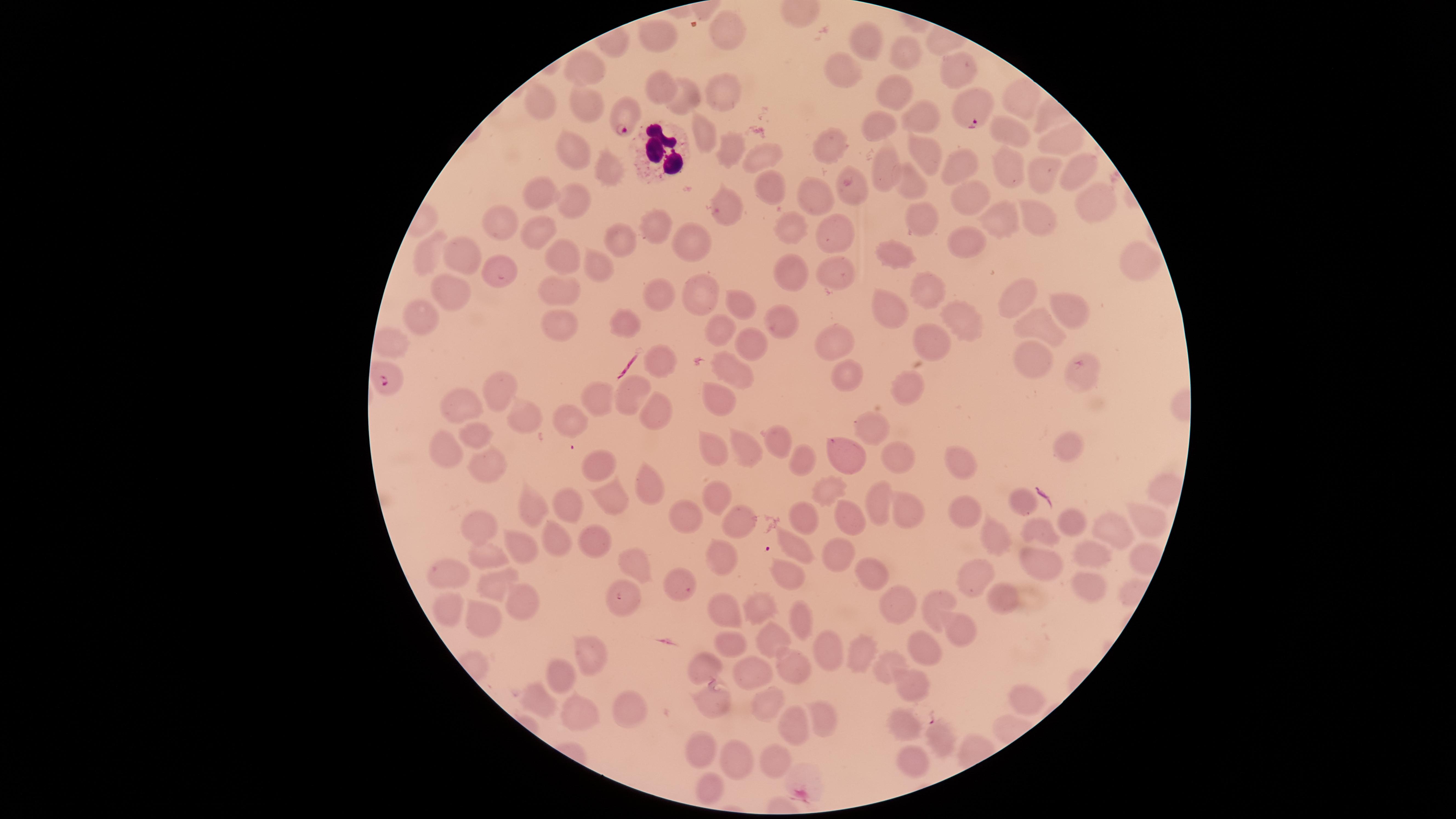
Approximate marker points as [x, y] in pixels. Parasitized RBCs: [970, 108], [623, 114], [388, 384]. Uninfected RBCs: [722, 32], [662, 37], [865, 41], [908, 54], [587, 67], [961, 67], [839, 70], [662, 85], [897, 93], [722, 94], [1019, 96], [685, 97], [538, 102], [588, 102], [923, 112], [1006, 123], [885, 124], [702, 131], [1059, 139], [829, 144], [572, 150], [922, 151], [728, 152], [760, 156], [613, 164], [889, 164], [962, 166], [1011, 169], [1074, 169], [1048, 176], [773, 183], [910, 183], [852, 191], [962, 193], [814, 195], [543, 196], [575, 196], [1100, 199], [724, 208], [1029, 215], [921, 216], [1002, 216], [510, 219], [794, 227], [844, 227], [656, 232], [548, 233], [621, 238], [693, 244], [967, 245], [896, 252], [465, 253], [428, 256], [1137, 257], [560, 261], [790, 265], [504, 267], [601, 269], [833, 274], [560, 290], [455, 292], [925, 292], [660, 293], [703, 293], [1023, 295], [736, 304], [1070, 307], [889, 310], [422, 314], [631, 317], [777, 320], [561, 323], [964, 325], [1040, 327], [719, 328], [834, 338], [752, 339], [925, 339], [392, 344], [1033, 356], [663, 359], [735, 368], [847, 376], [1082, 376], [908, 387], [498, 392], [633, 393], [721, 393], [598, 401], [464, 406], [657, 413], [526, 418], [575, 419], [869, 428], [481, 440], [779, 441], [713, 442], [1073, 447], [446, 449], [748, 451], [848, 456], [894, 460], [959, 460], [806, 462], [490, 463], [599, 466], [647, 485], [829, 490], [612, 494], [721, 497], [875, 498], [1019, 498], [533, 504], [570, 504], [964, 509], [906, 513], [685, 515], [804, 516], [852, 519], [1143, 519], [740, 520], [486, 523], [1068, 523], [553, 533], [1112, 535], [1044, 536], [596, 541], [992, 542], [520, 544], [798, 548], [1090, 553], [837, 554], [1034, 554], [484, 555], [719, 559], [635, 560], [977, 569], [448, 572], [874, 572], [790, 573], [495, 581], [677, 583], [1087, 588], [622, 594], [1004, 600], [938, 601], [524, 603], [761, 606], [897, 606], [449, 608], [727, 615], [481, 617], [799, 619], [964, 632], [772, 640], [734, 642], [858, 646], [593, 648], [924, 648], [829, 650], [706, 665], [795, 666], [750, 675], [883, 676], [553, 686], [918, 688], [1020, 698], [538, 699], [713, 702], [766, 704], [630, 715], [821, 715], [579, 720], [791, 726], [906, 728], [938, 739], [782, 753], [698, 754], [738, 758], [907, 763], [708, 790]. WBCs: [655, 147]. Presence: malaria parasites seen. Giemsa-stained preparation. Smartphone photograph through the microscope eyepiece. One field of view of the specimen. Species: Plasmodium falciparum. Circular visible region. Thin smear of blood. Image is 1456×819 pixels.